Report the malaria status of this cell.
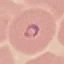
It is parasitized.

Summary:
  - Preparation: thin blood film
  - Image type: automatically extracted cell patch, resized to 64 × 64 pixels
  - Capture: smartphone through the microscope eyepiece
  - Stain: Giemsa